Locate every blood parasite and identify its species.
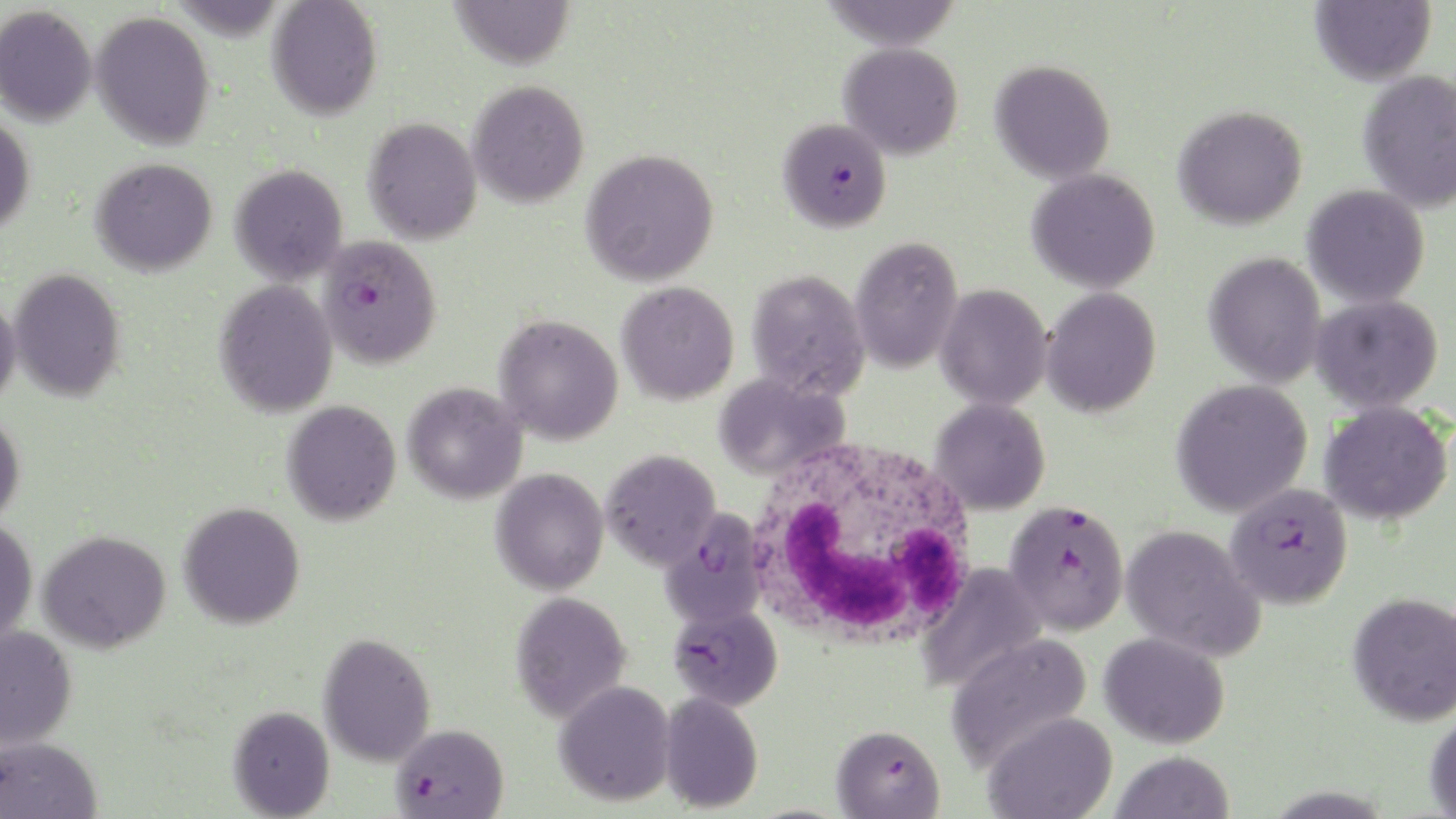
Approximate bounding boxes as (x1,y1)-(x2,y2) corner pairs in pixels.
Plasmodium falciparum-infected red blood cells: (778,117)-(892,233), (318,235)-(442,368), (1224,482)-(1352,610), (1004,499)-(1130,635), (660,507)-(768,628), (668,603)-(783,711), (390,724)-(509,819), (831,724)-(945,819).
No Plasmodium ovale, Plasmodium malariae, Plasmodium vivax, Babesia divergens, or Trypanosoma brucei observed.

slide-level diagnosis = Plasmodium falciparum
stain = May-Grünwald-Giemsa
preparation = thin blood film
image size = 1456×819 pixels
modality = optical microscopy
white blood cell locations = approximate bounding boxes as (x1,y1)-(x2,y2) corner pairs in pixels: (744,436)-(981,655)
field of view = single
uninfected red blood cell locations = approximate bounding boxes as (x1,y1)-(x2,y2) corner pairs in pixels: (266,0)-(383,120), (449,0)-(576,69), (817,0)-(964,50), (1310,0)-(1436,86), (0,5)-(97,127), (91,11)-(215,150), (838,43)-(964,160), (989,59)-(1116,184), (1357,70)-(1456,213), (468,80)-(590,208), (1172,104)-(1308,230), (0,114)-(35,236), (363,117)-(482,244), (580,148)-(719,287), (91,157)-(217,276), (230,163)-(348,286), (1026,168)-(1161,294), (1302,185)-(1430,308), (850,235)-(963,374), (1203,252)-(1327,388), (9,268)-(126,402), (746,268)-(871,399), (214,279)-(338,417), (617,281)-(739,405), (935,284)-(1053,410), (1041,287)-(1161,417), (0,294)-(20,409), (1311,295)-(1444,413), (494,314)-(624,445), (714,372)-(850,481), (1171,379)-(1313,517), (402,382)-(527,504), (930,398)-(1050,515), (282,400)-(401,526), (1320,401)-(1453,525), (0,409)-(25,527), (600,448)-(720,570), (491,468)-(609,595), (178,501)-(305,629), (0,517)-(38,647), (1120,524)-(1265,662), (37,529)-(170,653), (916,563)-(1046,693), (510,590)-(631,723), (1347,591)-(1456,726), (0,625)-(77,750), (1099,631)-(1230,749), (318,632)-(436,767), (946,632)-(1093,772), (554,680)-(676,807), (659,691)-(764,813), (228,704)-(334,818), (1425,710)-(1456,819), (984,711)-(1118,819), (0,736)-(102,819), (1111,750)-(1234,819)
magnification = 1000x